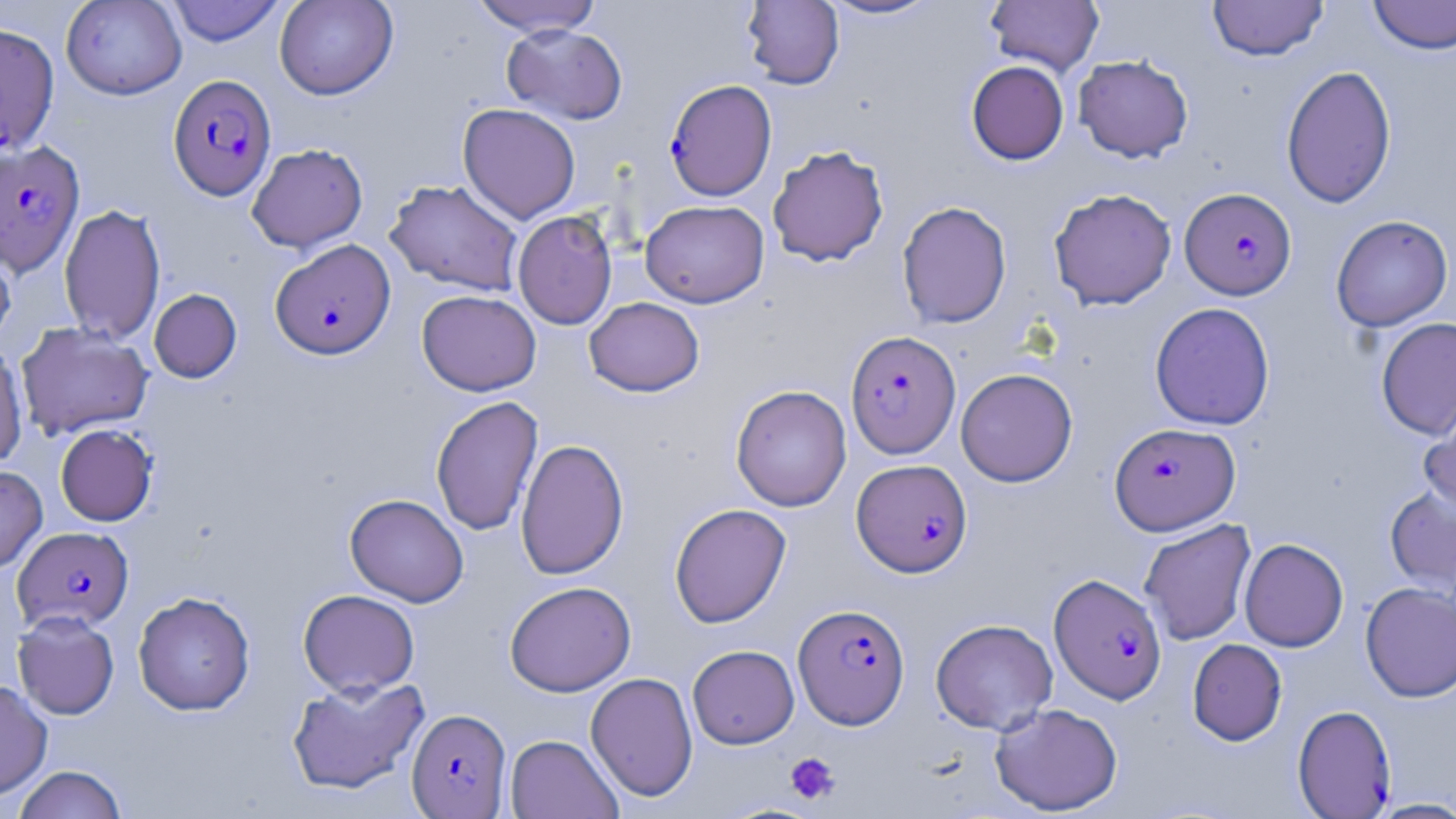

Approximate bounding boxes as (x1, y1, x2, y2) in pixels. Uninfected red blood cell locations: (61, 0, 186, 100), (166, 0, 285, 46), (274, 0, 398, 100), (469, 0, 603, 37), (820, 0, 942, 21), (985, 0, 1104, 76), (1208, 0, 1329, 61), (1367, 0, 1456, 55), (742, 1, 844, 89), (0, 22, 60, 157), (501, 24, 628, 125), (1073, 54, 1194, 163), (966, 60, 1069, 165), (1281, 64, 1397, 209), (457, 103, 581, 224), (246, 143, 368, 253), (767, 145, 889, 267), (384, 179, 524, 297), (1048, 188, 1177, 310), (640, 200, 770, 308), (896, 201, 1012, 329), (59, 204, 166, 343), (512, 210, 618, 329), (1331, 215, 1453, 332), (0, 235, 16, 352), (149, 288, 242, 383), (417, 289, 542, 396), (584, 297, 705, 396), (1149, 302, 1275, 430), (1376, 317, 1456, 440), (15, 322, 153, 440), (0, 341, 28, 467), (955, 368, 1078, 487), (730, 384, 852, 512), (430, 395, 543, 536), (1419, 395, 1456, 519), (55, 424, 158, 526), (515, 438, 629, 580), (0, 465, 48, 574), (1384, 484, 1456, 597), (345, 493, 469, 607), (669, 503, 791, 628), (1139, 519, 1257, 645), (1239, 538, 1349, 652), (504, 581, 636, 696), (1360, 581, 1456, 703), (298, 589, 420, 697), (132, 591, 255, 715), (12, 611, 119, 720), (930, 618, 1058, 734), (1187, 639, 1287, 745), (687, 644, 799, 748), (585, 672, 698, 802), (286, 676, 430, 796), (0, 679, 53, 800), (990, 703, 1123, 815), (505, 734, 623, 819), (13, 765, 127, 819), (1365, 798, 1456, 818). Platelet locations: (785, 752, 841, 805). Plasmodium falciparum-infected red blood cell locations: (168, 73, 277, 201), (664, 79, 777, 201), (0, 140, 85, 277), (1180, 187, 1297, 300), (270, 239, 396, 360), (845, 330, 960, 459), (1109, 422, 1240, 535), (851, 459, 973, 576), (13, 526, 133, 632), (1048, 573, 1167, 704), (793, 603, 910, 728), (1292, 704, 1396, 817), (406, 708, 510, 817). Slide-level diagnosis: Plasmodium falciparum. May-Grünwald-Giemsa stain. Light microscopy. One field of a larger specimen. Thin blood film. 1000x magnification. Image is 1456×819 pixels.